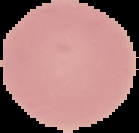
image_type: segmented cell region on a black background
image_size: 139×133 pixels
preparation: thin blood smear
malaria_status: uninfected